Outline each Plasmodium falciparum-infected red blood cell.
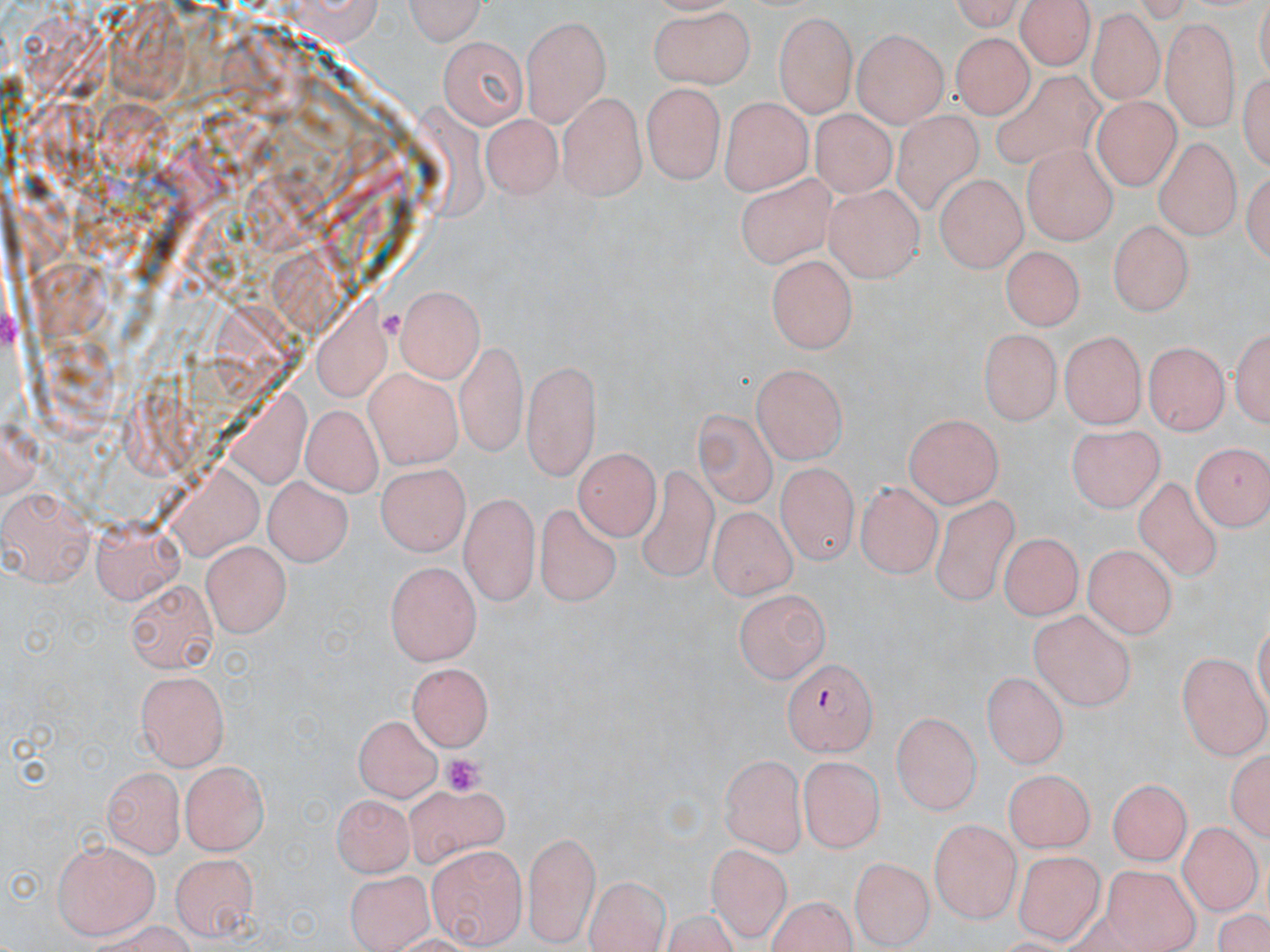

Approximate bounding boxes as (x1,y1)-(x2,y2) corner pairs in pixels.
Plasmodium falciparum-infected red blood cells: (782,660)-(875,755).

slide-level diagnosis = Plasmodium falciparum
uninfected red blood cell locations = approximate bounding boxes as (x1,y1)-(x2,y2) corner pairs in pixels: (942,0)-(1028,30), (1015,0)-(1097,70), (400,1)-(486,45), (647,5)-(758,89), (775,12)-(856,113), (1091,13)-(1162,99), (520,16)-(611,123), (1109,17)-(1216,117), (1160,18)-(1240,131), (854,30)-(948,126), (952,32)-(1029,120), (438,35)-(529,127), (1238,65)-(1267,178), (988,69)-(1110,167), (645,81)-(725,185), (558,90)-(644,198), (718,96)-(814,191), (1092,97)-(1178,190), (810,108)-(901,195), (889,109)-(987,220), (483,112)-(561,196), (1155,137)-(1240,239), (1022,144)-(1118,242), (734,170)-(839,273), (934,177)-(1031,269), (826,186)-(924,279), (1109,219)-(1191,318), (999,246)-(1088,328), (766,255)-(861,353), (392,285)-(485,380), (1233,318)-(1268,432), (1061,327)-(1147,428), (976,328)-(1060,425), (453,341)-(527,454), (1144,341)-(1225,437), (522,356)-(601,476), (749,364)-(849,464), (359,368)-(464,471), (298,403)-(380,496), (697,406)-(781,510), (901,412)-(1004,507), (1065,427)-(1164,513), (1192,443)-(1267,534), (574,450)-(659,539), (774,461)-(856,565), (375,464)-(470,556), (637,464)-(722,589), (1131,474)-(1227,587), (264,476)-(353,567), (856,482)-(940,578), (2,486)-(97,586), (933,489)-(1021,615), (458,491)-(537,609), (535,498)-(620,610), (707,506)-(798,600), (88,516)-(188,601), (997,530)-(1083,620), (200,539)-(289,635), (1081,547)-(1177,639), (384,558)-(480,662), (128,580)-(219,673), (735,587)-(831,682), (1029,610)-(1135,710), (1178,652)-(1269,755), (405,660)-(493,749), (135,671)-(232,768), (982,673)-(1066,771), (892,711)-(982,811), (354,713)-(445,801), (1228,745)-(1270,847), (719,753)-(807,856), (800,758)-(880,851), (178,761)-(272,856), (103,766)-(186,858), (1003,770)-(1097,850), (1106,776)-(1191,867), (85,785)-(179,924), (398,786)-(513,867), (332,794)-(410,878), (930,817)-(1021,925), (1181,823)-(1257,912), (523,829)-(601,944), (53,834)-(161,937), (425,842)-(526,945), (704,844)-(794,941), (1014,845)-(1102,943), (166,853)-(257,939), (851,856)-(931,948), (1104,865)-(1197,952), (343,866)-(433,951), (587,874)-(669,952), (764,898)-(860,952)
platelet locations = approximate bounding boxes as (x1,y1)-(x2,y2) corner pairs in pixels: (381,305)-(404,343), (438,752)-(486,797)
field of view = one of a larger specimen
preparation = thin blood film
stain = May-Grünwald-Giemsa
modality = optical microscopy
magnification = 1000x
image size = 1270×952 pixels